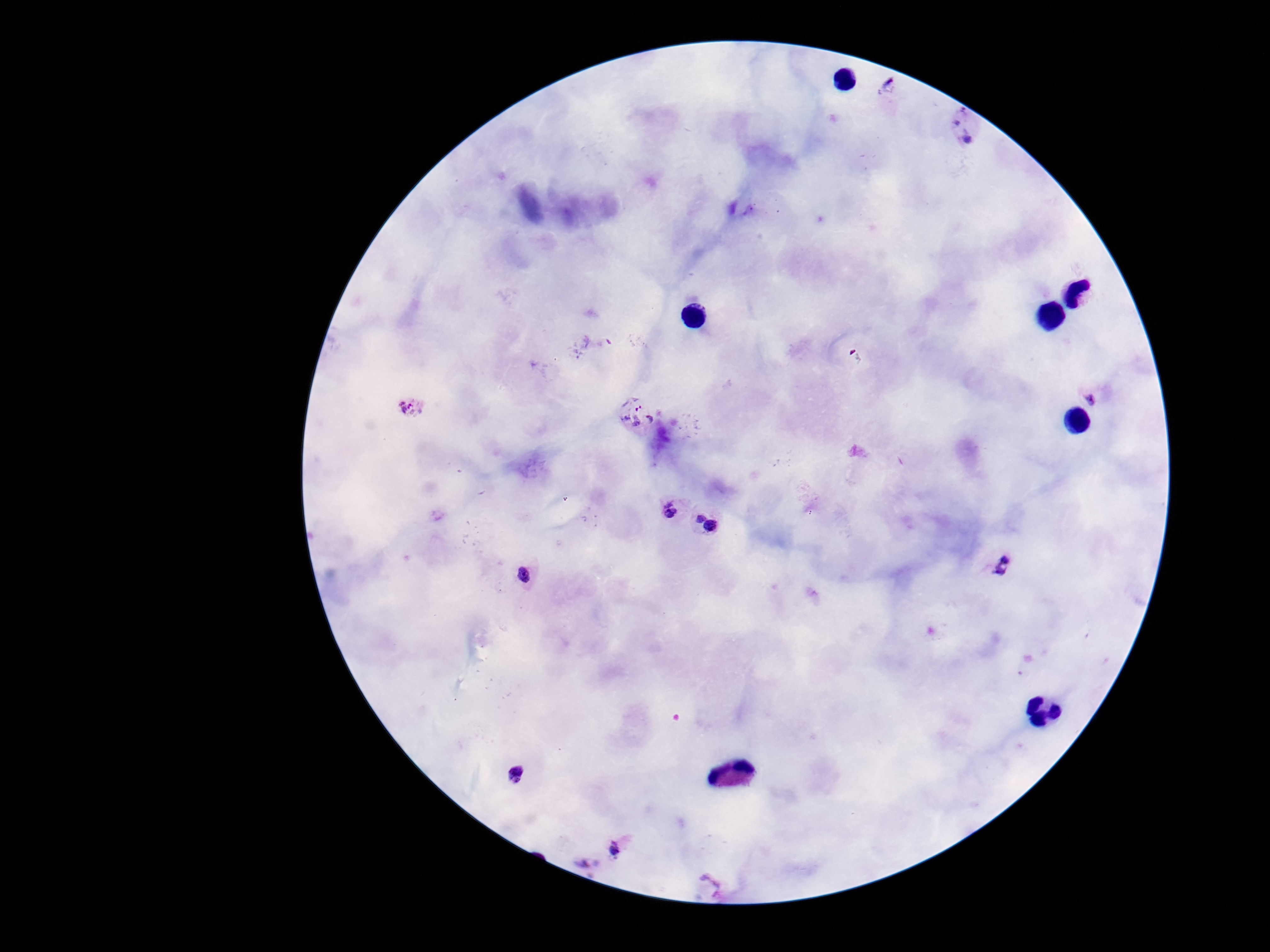

Approximate centers as [x, y] in pixels. Plasmodium parasite locations: [890, 85], [964, 127], [1098, 392], [412, 405], [638, 416], [666, 506], [710, 526], [999, 565], [525, 575], [514, 775], [621, 849], [584, 864], [710, 884]. 100x magnification. Photographed through the microscope eyepiece with a smartphone camera. Single field of view. Thick peripheral-blood smear. Giemsa-stained preparation. Image is 1270×952 pixels. Patient malaria status: positive.